Outline each Plasmodium falciparum-infected red blood cell.
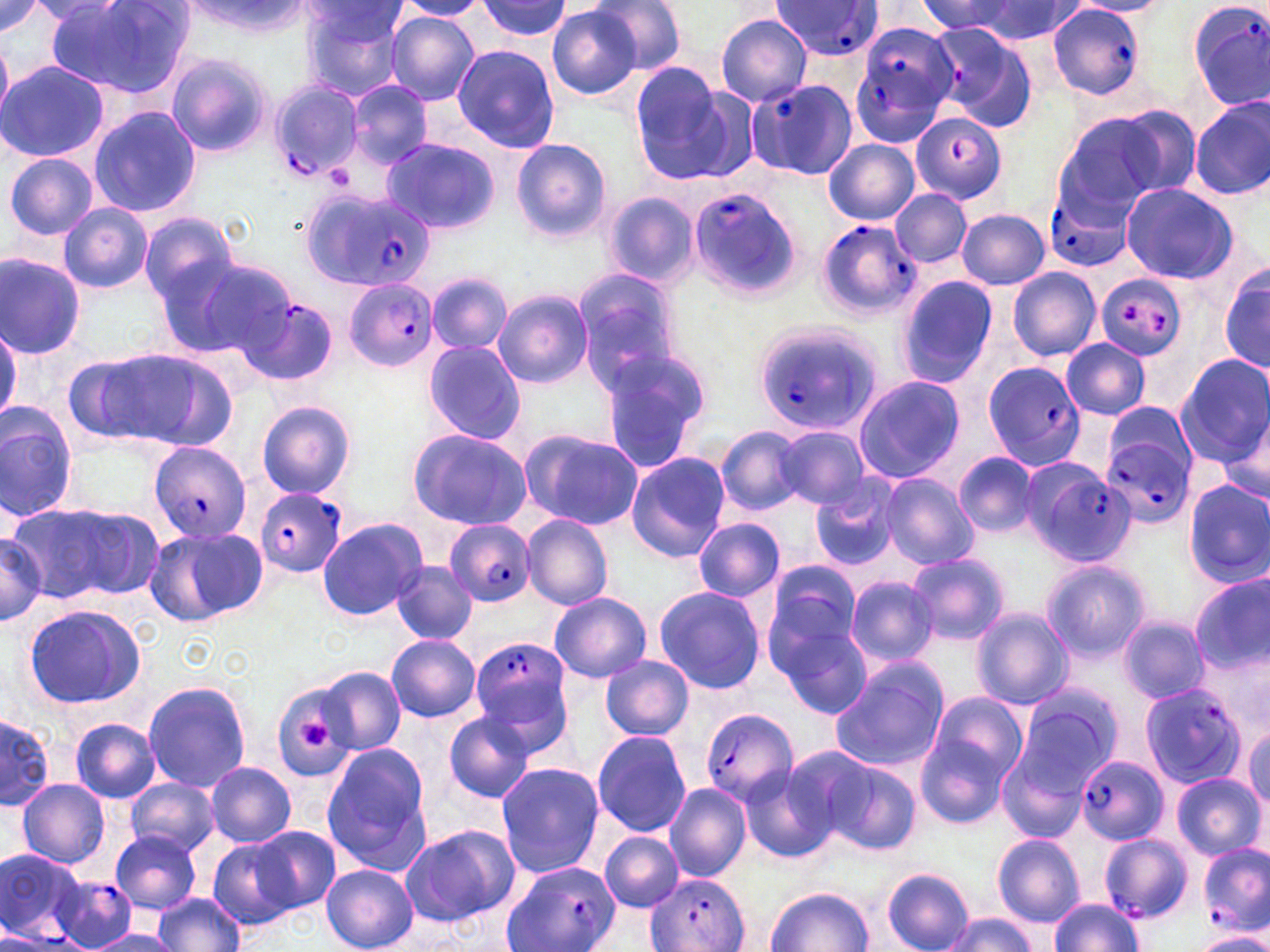
Approximate bounding boxes as (x1, y1, x2, y2) in pixels.
Plasmodium falciparum-infected red blood cells: (772, 0, 886, 60), (1185, 0, 1270, 110), (1047, 3, 1146, 100), (852, 18, 958, 149), (746, 77, 859, 181), (266, 81, 363, 183), (910, 111, 1006, 204), (299, 186, 426, 294), (688, 187, 803, 299), (1048, 191, 1128, 267), (817, 219, 920, 320), (1094, 274, 1188, 362), (344, 279, 438, 373), (233, 295, 337, 385), (753, 321, 882, 436), (984, 361, 1088, 470), (1101, 425, 1197, 526), (150, 442, 253, 542), (1027, 465, 1136, 568), (254, 488, 348, 577), (442, 519, 536, 607), (470, 636, 573, 744), (1141, 684, 1247, 789), (700, 708, 798, 808), (1076, 756, 1169, 845), (1101, 833, 1194, 923), (1201, 843, 1268, 935), (1, 849, 82, 943), (502, 860, 623, 952), (51, 873, 135, 949), (648, 873, 748, 952).

Summary:
  - Uninfected red blood cell locations: (0, 0, 44, 35), (588, 0, 689, 76), (45, 1, 192, 97), (395, 1, 488, 20), (473, 1, 575, 42), (965, 1, 1087, 44), (1070, 1, 1171, 17), (179, 2, 312, 38), (917, 2, 1035, 39), (301, 3, 411, 100), (548, 5, 644, 99), (384, 12, 480, 106), (715, 12, 812, 106), (922, 22, 1038, 132), (0, 38, 12, 116), (452, 44, 560, 152), (167, 55, 272, 156), (0, 60, 108, 163), (629, 62, 734, 177), (348, 80, 433, 169), (1190, 97, 1269, 201), (1105, 104, 1202, 198), (88, 107, 199, 220), (1055, 112, 1181, 212), (381, 137, 498, 234), (823, 138, 920, 225), (512, 139, 611, 243), (5, 153, 99, 241), (1119, 182, 1239, 284), (890, 188, 972, 268), (603, 190, 699, 289), (58, 202, 153, 293), (956, 209, 1051, 291), (139, 214, 242, 308), (0, 252, 87, 358), (169, 255, 297, 362), (1220, 263, 1270, 375), (1007, 267, 1101, 361), (573, 270, 682, 388), (426, 272, 512, 356), (896, 276, 997, 387), (493, 289, 593, 390), (1060, 339, 1149, 421), (422, 340, 526, 445), (116, 348, 238, 450), (598, 348, 712, 469), (62, 353, 165, 446), (1176, 354, 1270, 465), (853, 376, 965, 483), (255, 400, 357, 500), (0, 402, 78, 523), (1101, 402, 1196, 472), (1209, 410, 1270, 510), (775, 424, 870, 511), (716, 425, 808, 517), (407, 428, 530, 530), (518, 428, 642, 530), (953, 451, 1042, 539), (625, 452, 730, 562), (881, 472, 978, 571), (809, 475, 905, 574), (1183, 478, 1270, 586), (10, 501, 153, 605), (521, 514, 612, 611), (317, 518, 426, 622), (693, 518, 785, 602), (143, 526, 266, 627), (0, 529, 48, 627), (906, 552, 1010, 646), (1042, 560, 1150, 664), (390, 562, 477, 644), (759, 562, 861, 675), (1190, 574, 1270, 674), (846, 576, 940, 667), (652, 585, 766, 695), (549, 592, 652, 682), (24, 606, 145, 709), (971, 607, 1074, 710), (1118, 616, 1210, 702), (774, 622, 872, 719), (387, 635, 481, 721), (599, 656, 694, 740), (830, 657, 950, 772), (315, 664, 407, 759), (142, 681, 252, 792), (267, 681, 358, 782), (1009, 689, 1119, 805), (927, 690, 1028, 792), (1, 712, 52, 811), (443, 712, 536, 802), (914, 718, 1019, 830), (70, 719, 161, 803), (1245, 723, 1270, 812), (591, 729, 692, 838), (322, 744, 434, 874), (1000, 748, 1088, 847), (818, 755, 923, 856), (205, 761, 297, 846), (495, 762, 604, 877), (739, 763, 839, 864), (1172, 772, 1263, 859), (17, 778, 110, 868), (125, 778, 219, 856), (664, 784, 753, 881), (400, 823, 518, 927), (251, 825, 339, 914), (111, 831, 202, 913), (600, 832, 684, 912), (993, 834, 1084, 927), (209, 838, 297, 928), (321, 865, 418, 952), (882, 868, 974, 952), (767, 888, 873, 951), (153, 893, 244, 951), (1048, 897, 1144, 951), (943, 912, 1037, 952), (0, 929, 76, 952), (88, 931, 184, 952), (1195, 931, 1270, 952)
  - Platelet locations: (328, 165, 353, 185), (294, 717, 334, 752)
  - Slide-level diagnosis: Plasmodium falciparum
  - Preparation: thin blood film
  - Stain: May-Grünwald-Giemsa
  - Modality: light microscopy
  - Field of view: single
  - Image size: 1270×952 pixels
  - Magnification: 1000x